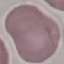
Summary:
  - Malaria status: uninfected
  - Capture: smartphone camera at the microscope eyepiece
  - Stain: Giemsa
  - Image type: cell patch, automatically extracted from a larger field of view and resized to 64 × 64 pixels
  - Preparation: thin smear